Report the malaria status of this cell.
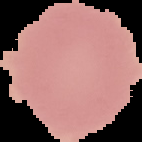
Uninfected.

preparation = thin blood film
image type = segmented cell region on a black background
image size = 142×142 pixels